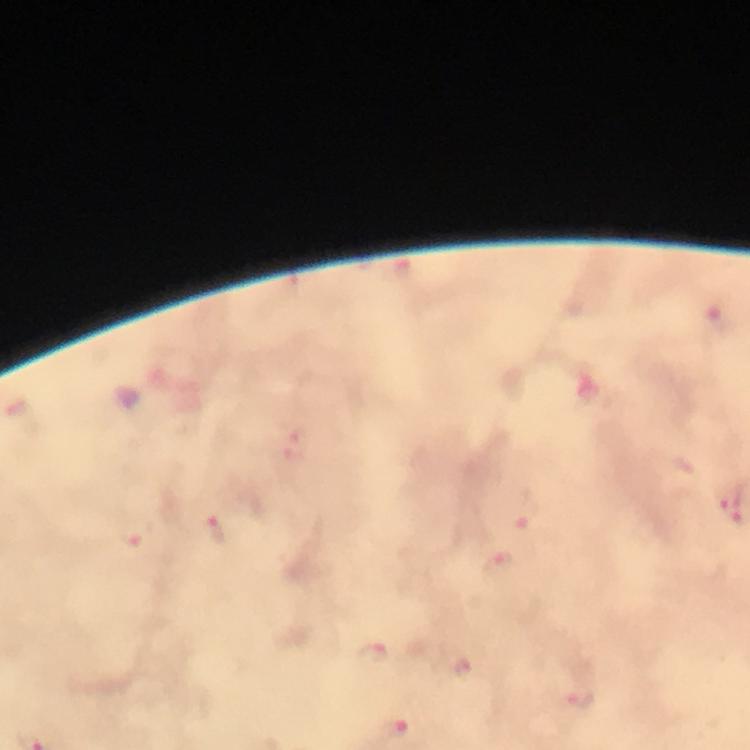

stain: Giemsa
context: from a diagnostic examination for malaria
cropped_from: a single field of view
immersion_oil: used
malaria_parasite_locations: 'approximate centers as (x, y) in pixels: (717, 319), (298, 444), (732, 503), (528, 516), (221, 533), (136, 534), (499, 565), (372, 653), (584, 697), (398, 729)'
capture: smartphone mounted on the microscope
magnification: 100x
preparation: thick blood film
image_size: 750×750 pixels